Identify the parasite.
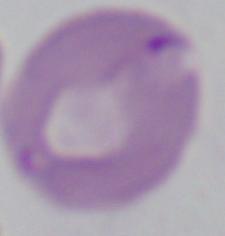

Babesia.

Captured at 1000x magnification. Photomicrograph.